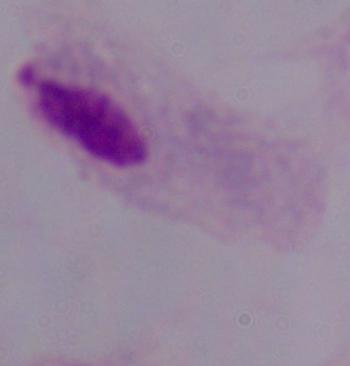

Summary:
  - Modality: micrograph
  - Identification: trichomonad
  - Magnification: 1000x